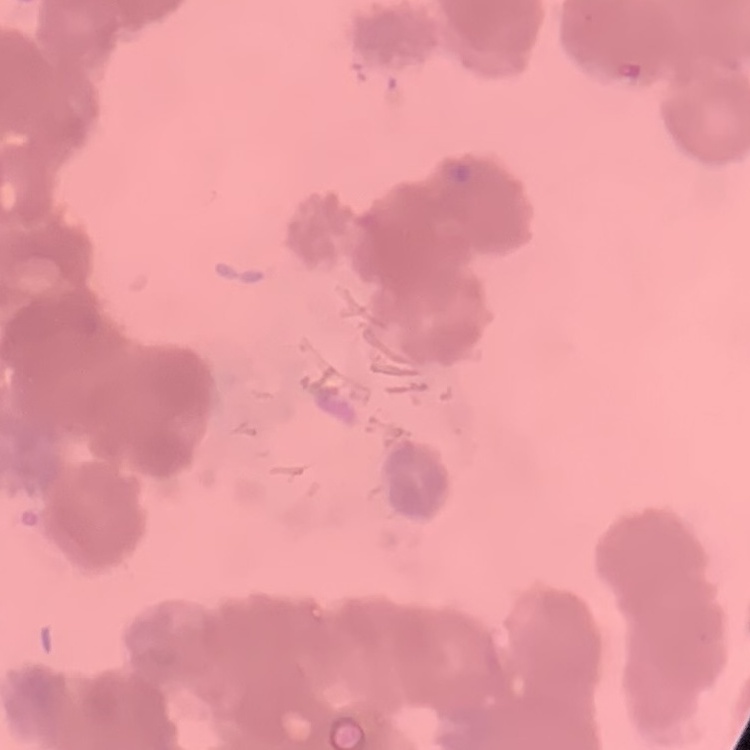 The red blood cells show rouleaux formation. Square crop of a larger photomicrograph. Stained with either Field's or Giemsa. Thin blood smear.